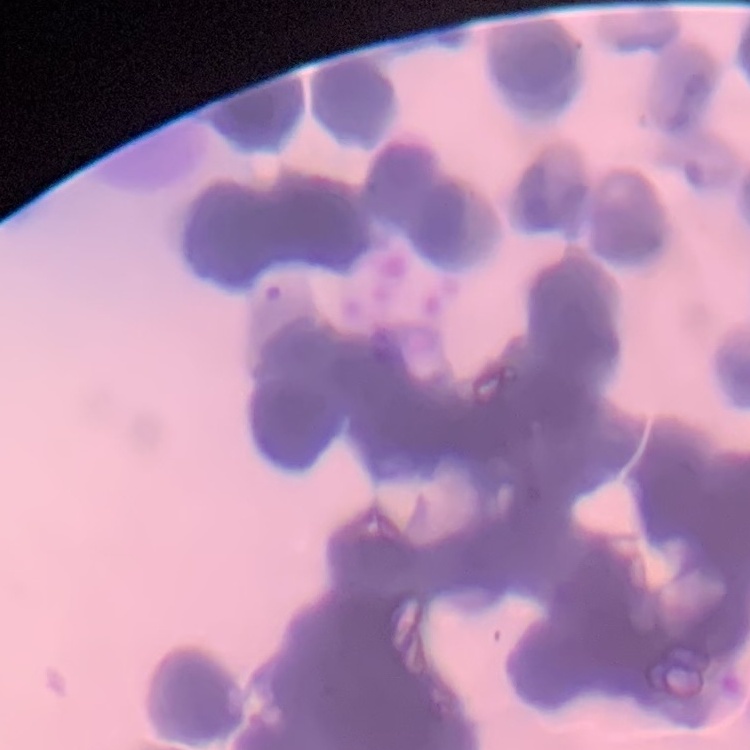
Summary:
  - Red blood cell morphology: rouleaux formation
  - Preparation: thin peripheral smear
  - Stain: Field's or Giemsa
  - Image type: one tile cut from a larger photomicrograph